State which cell type is depicted.
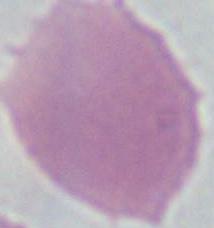

An erythrocyte.

Summary:
  - Modality: micrograph
  - Magnification: 1000x